Report the malaria status of this cell.
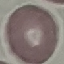

Uninfected.

Summary:
  - Capture: smartphone camera at the microscope eyepiece
  - Preparation: thin blood film
  - Stain: Giemsa
  - Image type: automatically extracted cell patch, resized to 64 × 64 pixels